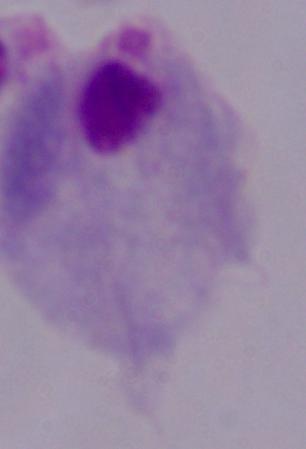

Summary:
  - Modality: micrograph
  - Identification: trichomonad
  - Magnification: 1000x